Assess this cell for malaria.
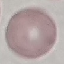

Uninfected.

Summary:
  - Capture: smartphone camera at the microscope eyepiece
  - Stain: Giemsa
  - Image type: automatically extracted cell patch, resized to 64 × 64 pixels
  - Preparation: thin smear